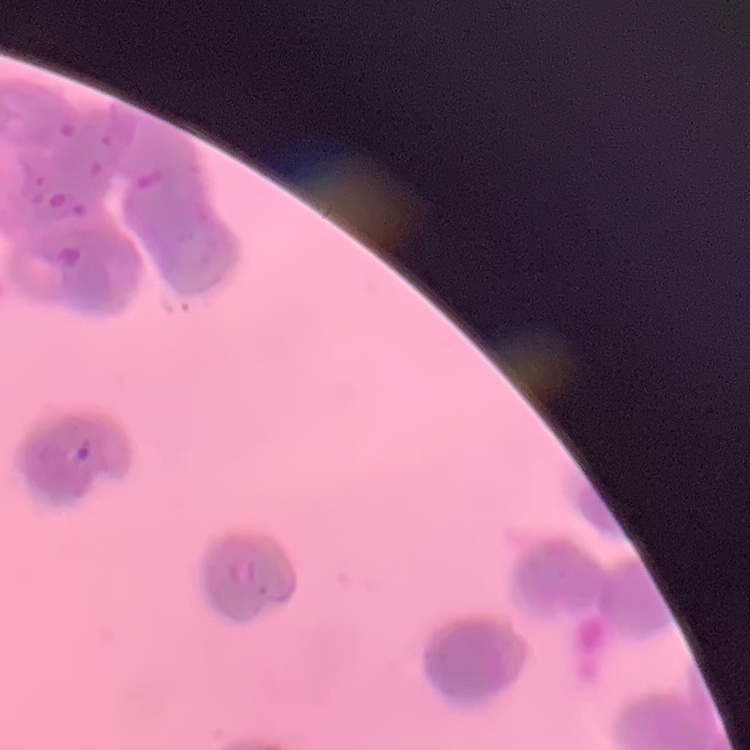

{
  "red_blood_cell_morphology": "rouleaux formation",
  "preparation": "thin blood film",
  "image_type": "square crop of a larger photomicrograph",
  "stain": "Field's or Giemsa"
}